Identify the parasite.
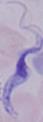

This is a trypanosome.

1000x magnification. Photomicrograph.